Report the malaria status of this cell.
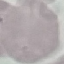
Uninfected.

Giemsa stain. Thin blood film. Cell patch, automatically extracted from a larger field of view and resized to 64 × 64 pixels. Acquired by smartphone through the microscope eyepiece.